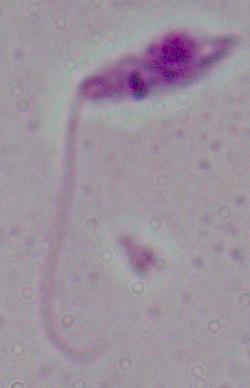
Summary:
  - Modality: photomicrograph
  - Identification: Leishmania
  - Magnification: 1000x